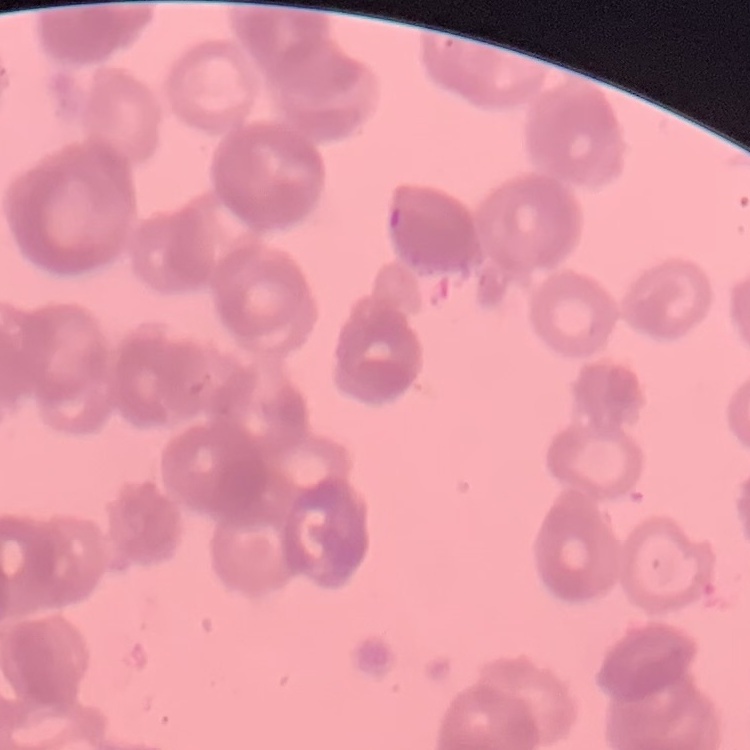
erythrocyte_morphology: rouleaux formation
image_type: one tile cut from a larger photomicrograph
preparation: thin blood film
stain: Field's or Giemsa